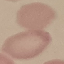

result = no malaria parasites seen
stain = Giemsa
image type = automatically extracted cell patch, resized to 64 × 64 pixels
preparation = thin blood film
capture = smartphone camera at the microscope eyepiece